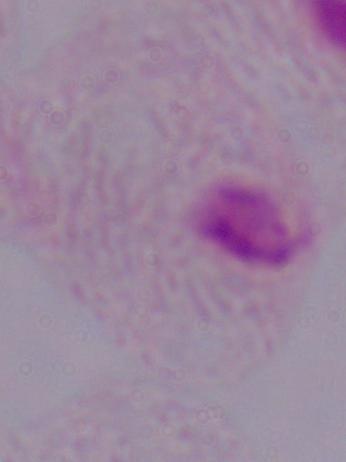
identification = trichomonad
modality = photomicrograph
magnification = 1000x